Identify the blood parasite species.
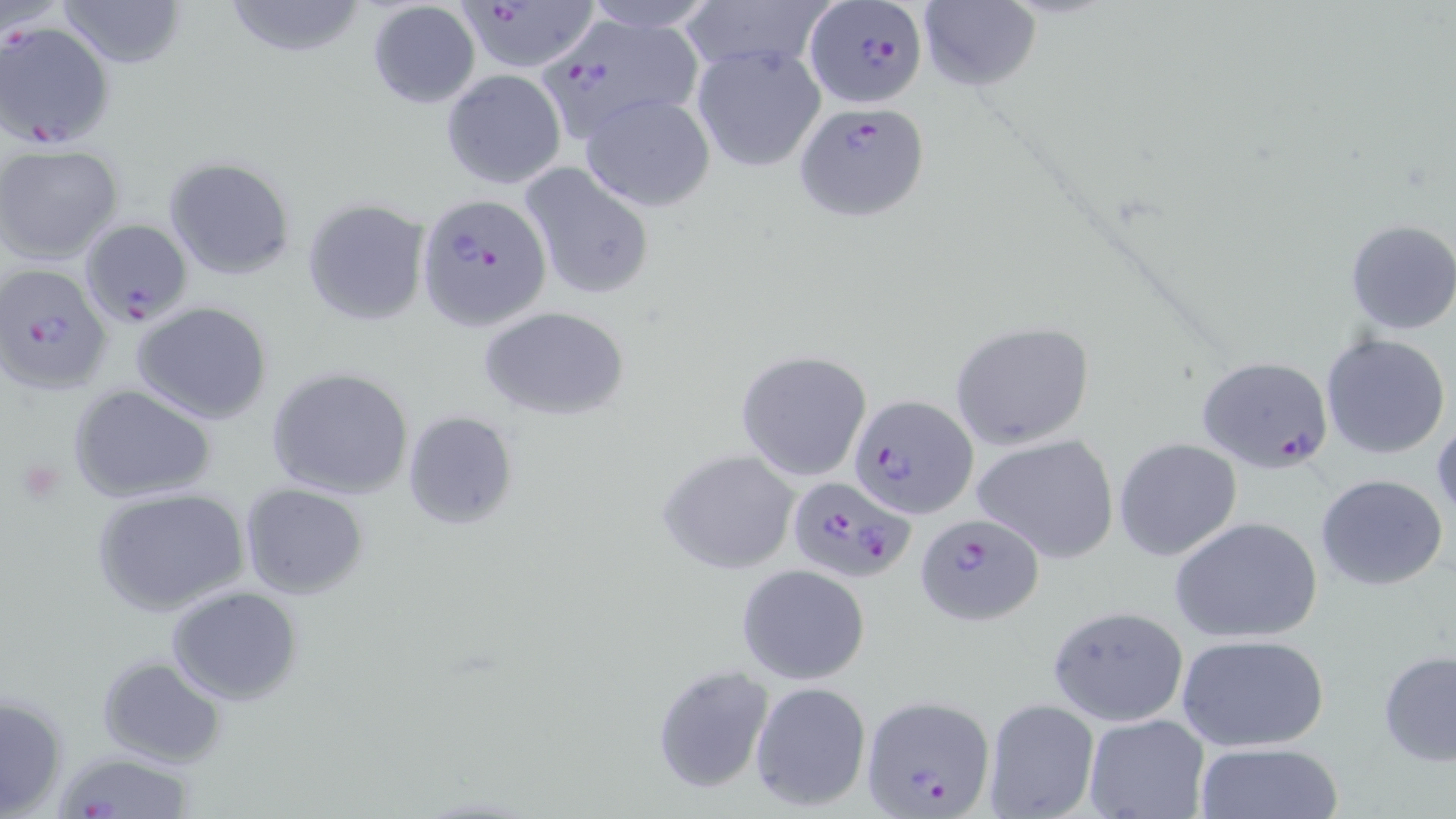

Plasmodium falciparum.

Approximate bounding boxes as (x1,y1)-(x2,y2) corner pairs in pixels. Uninfected red blood cell locations: (56,0)-(187,70), (221,0)-(370,59), (683,0)-(829,78), (364,1)-(481,108), (575,1)-(720,33), (916,1)-(1042,92), (689,42)-(828,172), (441,70)-(567,189), (579,92)-(715,212), (0,145)-(125,262), (163,156)-(295,280), (517,161)-(656,302), (302,198)-(431,327), (1343,219)-(1456,336), (132,302)-(272,423), (481,307)-(628,420), (949,321)-(1097,450), (1321,333)-(1452,460), (737,350)-(871,482), (267,366)-(414,500), (68,383)-(217,503), (403,410)-(517,531), (1431,414)-(1455,524), (971,433)-(1119,563), (1113,438)-(1241,560), (659,449)-(801,575), (1315,474)-(1450,593), (239,483)-(370,599), (90,487)-(251,617), (1170,516)-(1323,643), (737,562)-(870,684), (165,586)-(303,705), (1048,605)-(1189,726), (1174,632)-(1332,752), (1379,650)-(1456,767), (97,655)-(227,768), (652,663)-(774,794), (749,680)-(873,813), (1,692)-(70,819), (983,698)-(1100,818), (1084,714)-(1209,819), (1193,742)-(1344,819). Plasmodium falciparum-infected red blood cell locations: (457,2)-(595,70), (804,2)-(928,110), (1,19)-(116,148), (550,22)-(710,142), (796,103)-(930,219), (416,193)-(553,331), (80,217)-(193,329), (0,263)-(113,395), (1194,356)-(1335,474), (848,393)-(976,521), (784,475)-(914,583), (916,513)-(1042,624), (861,697)-(996,819), (53,750)-(201,818). Platelet locations: (14,457)-(64,504). Optical microscopy. May-Grünwald-Giemsa-stained preparation. Thin blood smear. One field of a larger specimen. 1000x magnification. Image is 1456×819 pixels.